Report the malaria status of this cell.
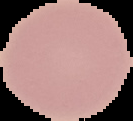

It is uninfected.

Segmented cell region on a black background. From a thin blood film. Image is 133×121 pixels.